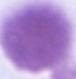
Captured at 1000x magnification. Photomicrograph. A red blood cell is seen.